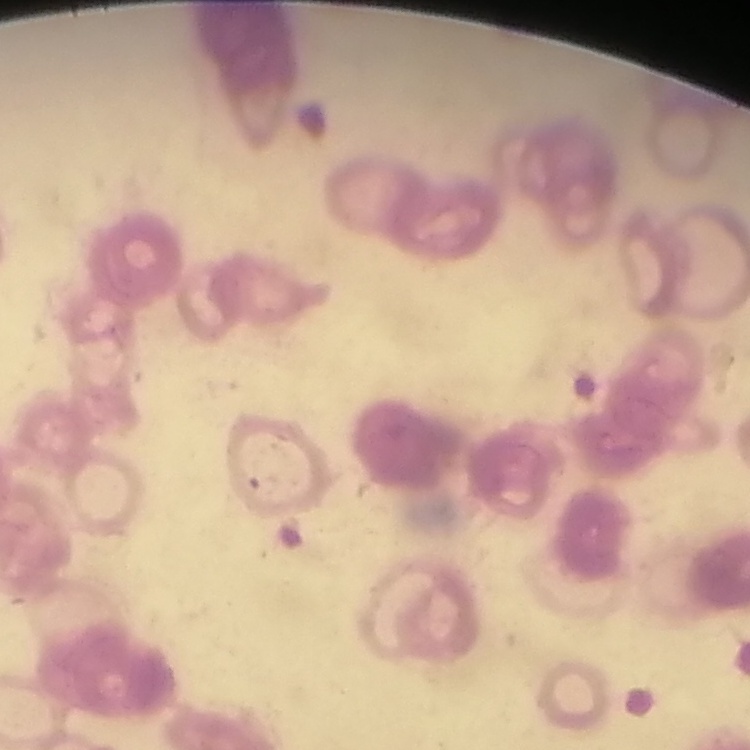 The red blood cells exhibit rouleaux formation. Thin blood film. Stained with either Field's or Giemsa. One tile cut from a larger photomicrograph.